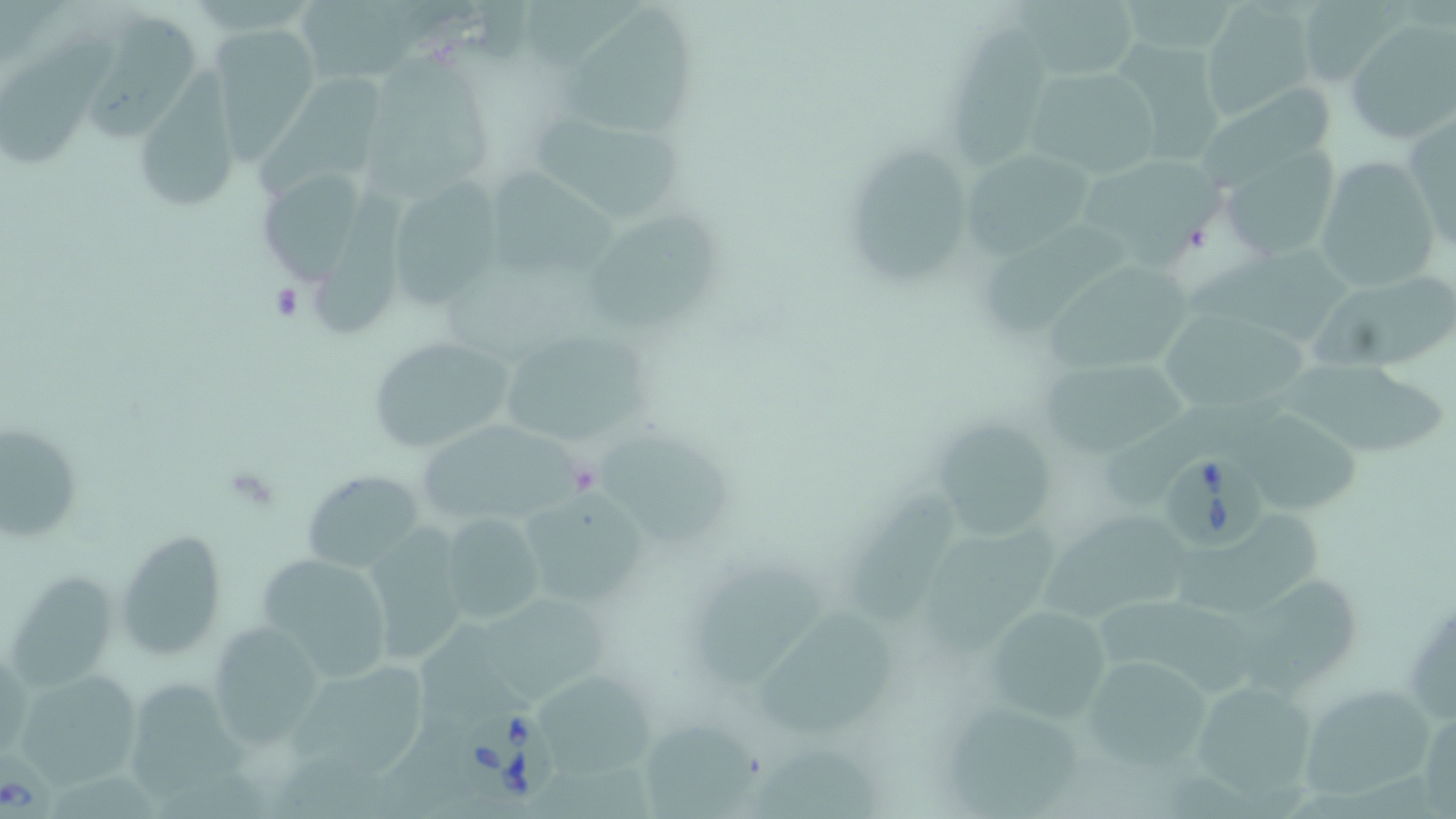

slide-level diagnosis = Babesia divergens
field of view = one of a larger specimen
platelet locations = approximate bounding boxes as (x1, y1, x2, y2) in pixels: (270, 282, 304, 322)
image size = 1456×819 pixels
Babesia divergens-infected red blood cell locations = approximate bounding boxes as (x1, y1, x2, y2) in pixels: (1163, 449, 1264, 553), (457, 708, 567, 810)
preparation = thin blood smear
modality = light microscopy
stain = May-Grünwald-Giemsa
magnification = 1000x
uninfected red blood cell locations = approximate bounding boxes as (x1, y1, x2, y2) in pixels: (1014, 0, 1143, 82), (1127, 0, 1236, 51), (524, 1, 652, 71), (300, 3, 408, 81), (1198, 3, 1315, 120), (1301, 3, 1411, 89), (556, 5, 705, 139), (89, 10, 195, 140), (1345, 19, 1456, 146), (4, 23, 117, 170), (207, 27, 318, 159), (950, 28, 1053, 180), (1110, 39, 1230, 166), (358, 51, 497, 198), (136, 60, 245, 210), (1025, 65, 1160, 177), (255, 67, 379, 192), (1186, 79, 1349, 194), (531, 111, 683, 225), (1405, 113, 1456, 252), (840, 138, 979, 292), (958, 147, 1097, 257), (1223, 147, 1341, 262), (1085, 150, 1235, 268), (1314, 156, 1441, 294), (494, 168, 620, 277), (255, 171, 359, 286), (397, 179, 503, 312), (317, 193, 412, 339), (589, 211, 722, 330), (984, 218, 1128, 341), (1184, 244, 1356, 342), (1045, 257, 1196, 371), (1312, 274, 1456, 368), (1163, 313, 1318, 411), (495, 326, 648, 450), (365, 335, 519, 454), (1280, 355, 1446, 456), (1043, 359, 1191, 456), (1099, 402, 1246, 508), (1243, 413, 1359, 518), (928, 418, 1062, 539), (1, 422, 83, 543), (419, 423, 594, 525), (593, 430, 736, 548), (301, 470, 427, 571), (847, 485, 961, 626), (517, 491, 647, 610), (1174, 509, 1329, 615), (442, 512, 546, 626), (1040, 512, 1198, 619), (920, 515, 1062, 658), (358, 524, 472, 667), (115, 530, 229, 661), (254, 553, 395, 682), (687, 566, 840, 681), (10, 571, 119, 691), (1236, 578, 1366, 697), (475, 586, 609, 699), (1101, 592, 1264, 703), (982, 604, 1114, 720), (761, 607, 898, 743), (208, 621, 329, 741), (421, 626, 533, 737), (292, 654, 430, 781), (1080, 656, 1213, 774), (12, 668, 147, 786), (543, 673, 661, 778), (1190, 679, 1326, 807), (133, 680, 254, 801), (1296, 681, 1438, 803), (945, 702, 1086, 819), (641, 710, 762, 819), (747, 748, 885, 819)